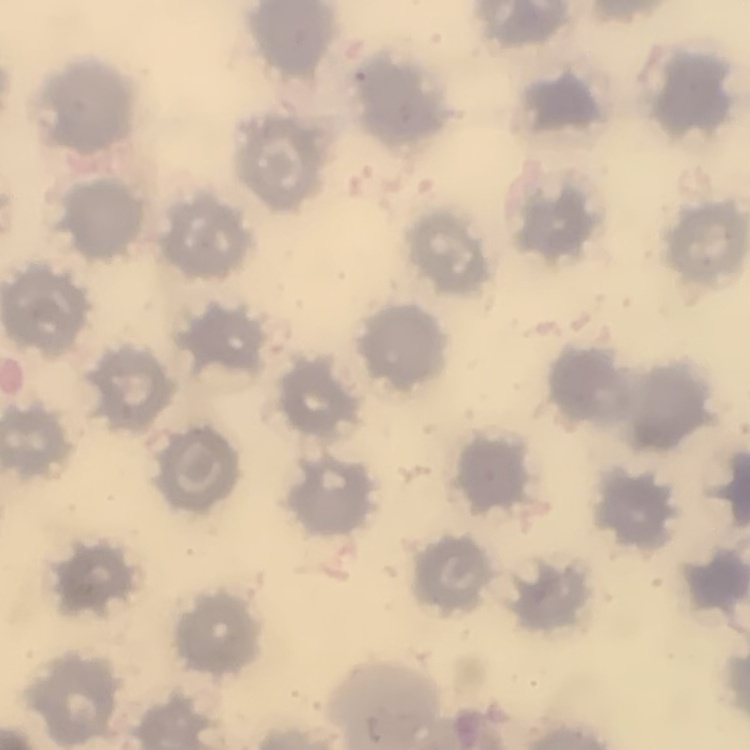

Summary:
  - Red blood cell morphology: no rouleaux formation
  - Preparation: thin blood film
  - Image type: square crop of a larger photomicrograph
  - Stain: Field's or Giemsa